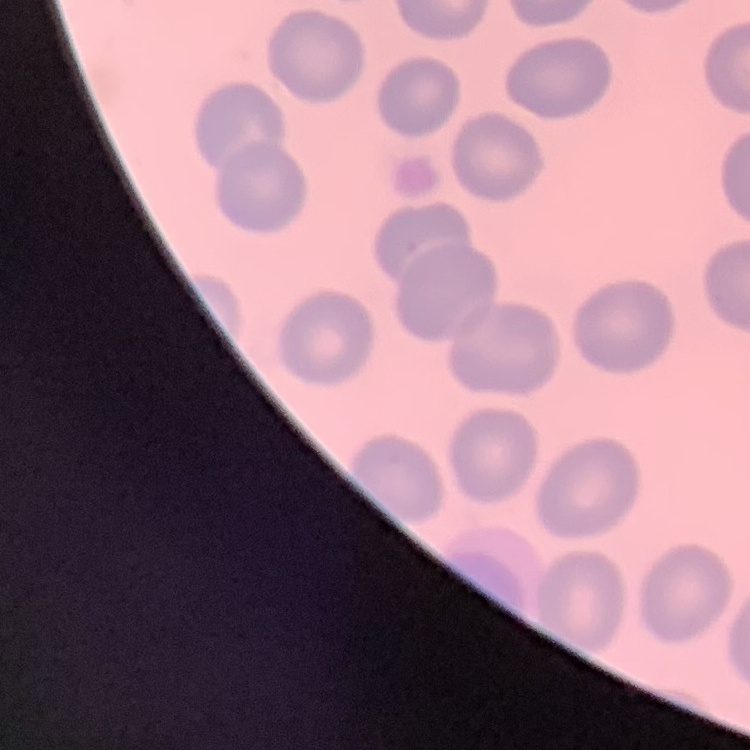

erythrocyte_morphology: no rouleaux formation
preparation: thin blood film
stain: Field's or Giemsa
image_type: one tile cut from a larger photomicrograph